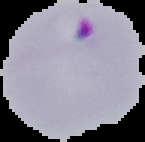

malaria status = parasitized
image size = 145×142 pixels
preparation = thin blood film
image type = cell region segmented out of the field of view; surrounding area masked to black